Classify this cell by malaria status.
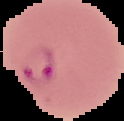
It is parasitized.

Summary:
  - Image type: segmented cell region on a black background
  - Image size: 124×121 pixels
  - Preparation: thin blood film